Assess this cell for malaria.
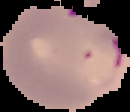

It is parasitized.

Segmented cell region on a black background. Image is 130×112 pixels. From a thin blood smear.